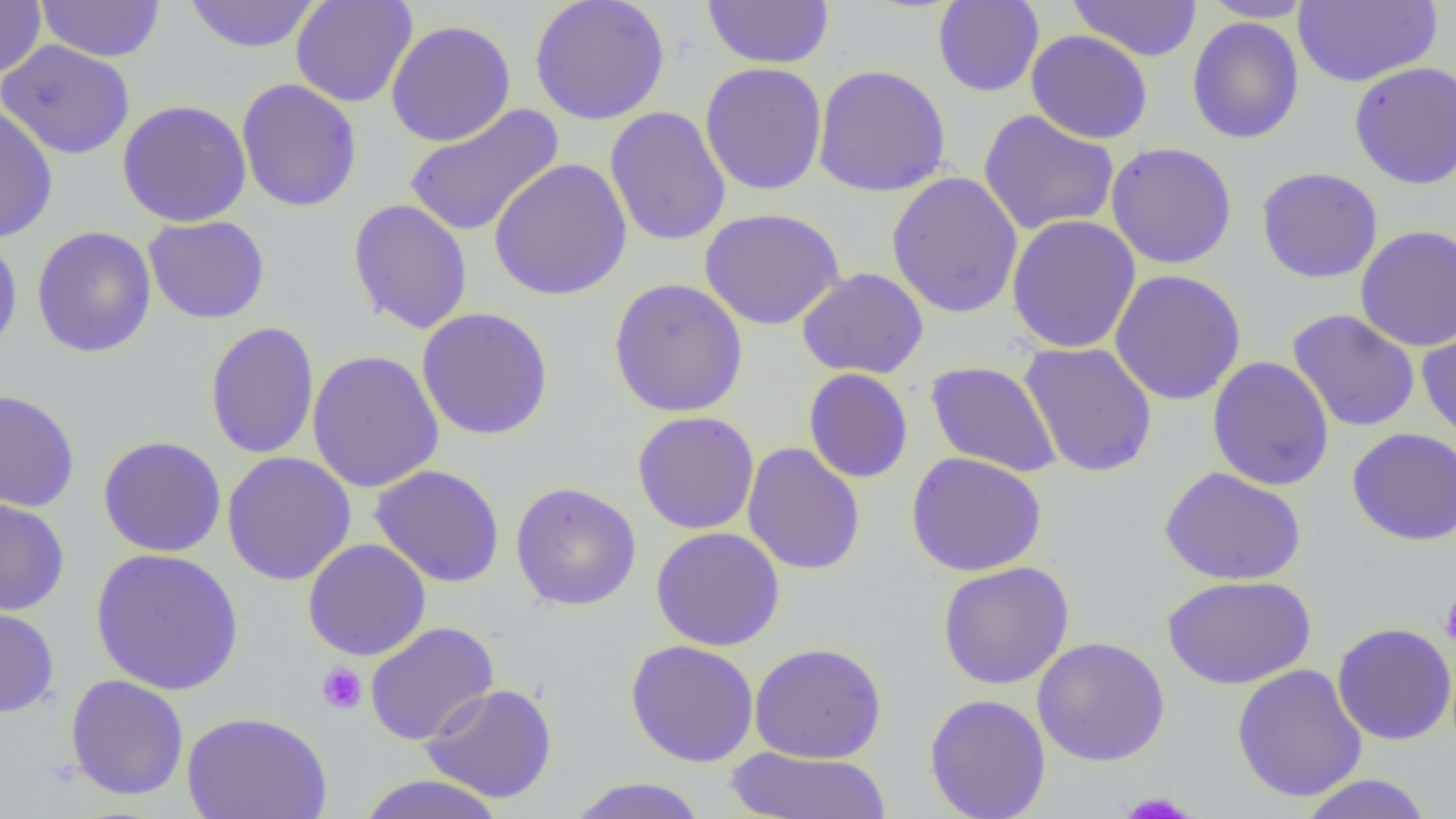
Summary:
  - Coordinate format: approximate bounding boxes as (x1,y1)-(x2,y2) corner pairs in pixels
  - Platelet locations: (1440,590)-(1456,651), (316,662)-(368,715), (1118,791)-(1197,818)
  - Uninfected red blood cell locations: (0,0)-(46,80), (36,0)-(165,62), (183,0)-(322,53), (290,0)-(418,108), (529,0)-(670,126), (702,0)-(834,69), (1067,0)-(1203,62), (1200,0)-(1316,22), (932,1)-(1045,98), (1294,1)-(1442,87), (1187,16)-(1304,144), (386,19)-(516,147), (1026,29)-(1153,144), (0,40)-(135,160), (1349,61)-(1456,190), (700,62)-(827,196), (812,64)-(951,197), (236,79)-(362,212), (116,99)-(252,227), (404,102)-(564,238), (0,104)-(58,243), (605,106)-(731,247), (978,110)-(1120,236), (1106,142)-(1238,269), (488,157)-(632,302), (1256,166)-(1383,283), (886,171)-(1024,319), (348,198)-(473,335), (699,207)-(845,330), (1006,214)-(1141,354), (143,215)-(270,324), (1355,225)-(1456,352), (31,226)-(157,358), (0,231)-(23,360), (797,268)-(929,379), (1109,269)-(1247,406), (608,277)-(748,418), (416,307)-(554,441), (1287,309)-(1420,433), (1417,318)-(1456,446), (205,321)-(320,460), (1019,342)-(1158,478), (306,349)-(445,493), (1207,356)-(1335,491), (925,360)-(1062,477), (803,367)-(913,483), (0,389)-(80,512), (631,411)-(760,535), (1347,427)-(1456,546), (97,435)-(227,557), (742,443)-(866,575), (222,451)-(357,586), (906,452)-(1047,576), (369,464)-(505,588), (1159,467)-(1305,585), (510,481)-(641,611), (0,494)-(70,616), (651,526)-(785,651), (302,539)-(431,661), (90,547)-(245,696), (937,561)-(1074,690), (1161,573)-(1316,689), (0,605)-(60,718), (365,621)-(499,746), (1332,622)-(1456,745), (1032,636)-(1170,766), (625,639)-(759,767), (748,642)-(887,763), (1231,663)-(1368,802), (64,674)-(190,801), (420,683)-(558,803), (924,693)-(1051,819), (181,710)-(334,819), (725,747)-(892,818), (354,774)-(509,819), (1298,774)-(1433,819), (566,777)-(710,819)
  - Slide-level diagnosis: no evidence of blood parasites
  - Field of view: one of a larger specimen
  - Image size: 1456×819 pixels
  - Magnification: 1000x
  - Preparation: thin blood film
  - Modality: optical microscopy